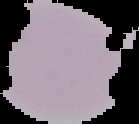
image_size: 139×124 pixels
result: no malaria parasites seen
preparation: thin blood smear
image_type: cell region segmented out of the field of view; surrounding area masked to black